Outline each blood parasite and name the species.
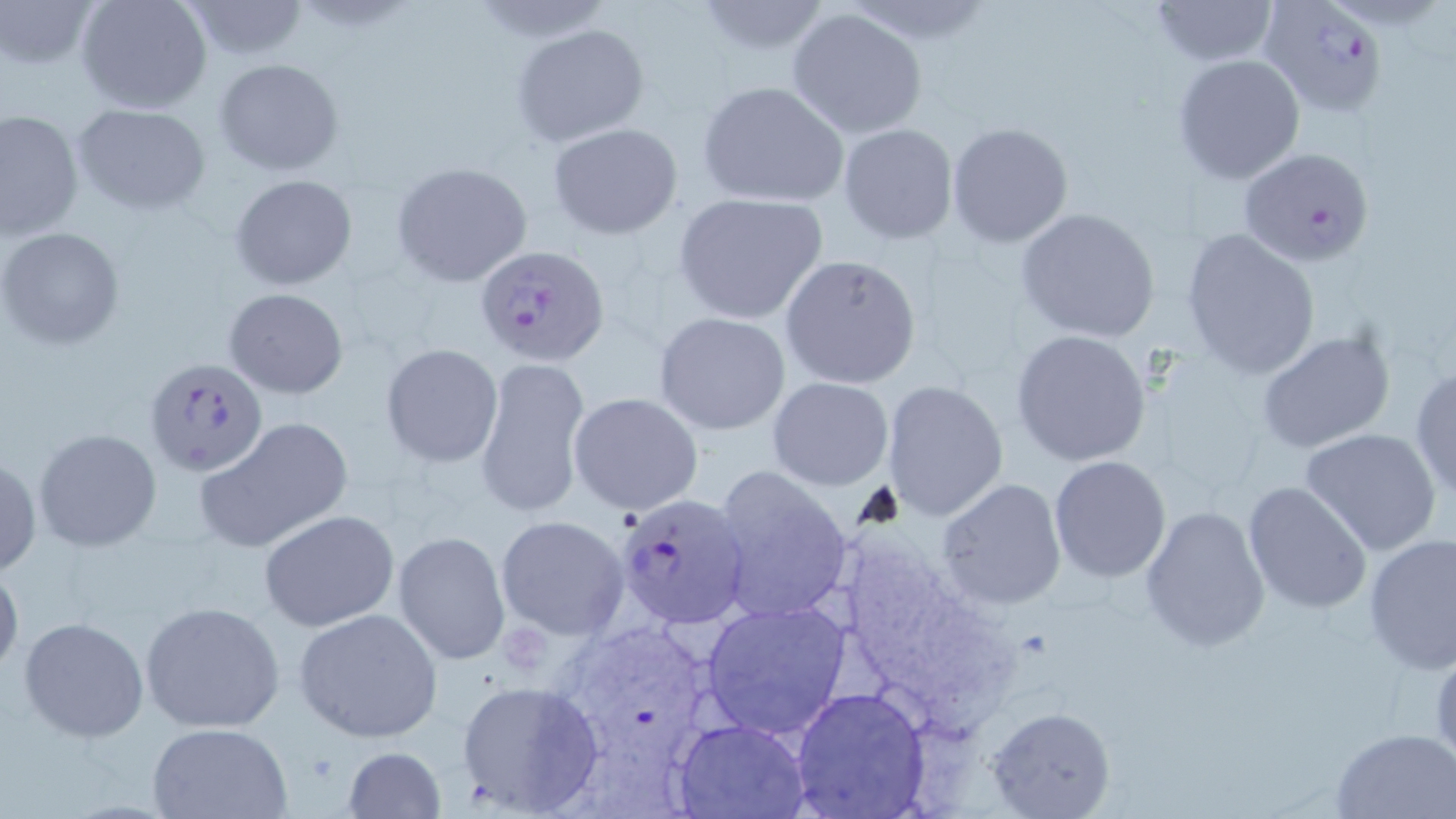

Approximate bounding boxes as (x1, y1, x2, y2) in pixels.
Plasmodium falciparum-infected red blood cells: (1260, 0, 1389, 116), (1237, 145, 1374, 265), (476, 246, 609, 366), (145, 358, 269, 476), (616, 493, 750, 629).
No Plasmodium ovale, Plasmodium malariae, Plasmodium vivax, Babesia divergens, or Trypanosoma brucei observed.

Summary:
  - Uninfected red blood cell locations: (2, 0, 103, 71), (75, 0, 213, 114), (1149, 0, 1277, 67), (179, 1, 309, 61), (690, 1, 830, 55), (788, 7, 929, 138), (513, 24, 650, 146), (1172, 53, 1305, 185), (214, 57, 344, 176), (696, 81, 849, 208), (72, 104, 210, 215), (0, 107, 84, 242), (548, 122, 684, 239), (946, 123, 1073, 248), (837, 124, 959, 244), (391, 163, 533, 287), (230, 173, 358, 290), (672, 192, 829, 325), (1014, 207, 1161, 343), (0, 226, 125, 351), (1180, 229, 1320, 379), (779, 254, 922, 389), (223, 287, 349, 400), (653, 311, 790, 435), (1257, 329, 1396, 454), (1011, 330, 1150, 466), (381, 343, 503, 467), (477, 355, 591, 522), (1409, 364, 1456, 500), (769, 377, 894, 489), (882, 381, 1009, 520), (569, 392, 704, 515), (197, 416, 354, 552), (1301, 427, 1442, 555), (33, 428, 163, 553), (1, 454, 42, 581), (1049, 457, 1170, 581), (709, 465, 852, 623), (938, 477, 1066, 610), (1242, 481, 1371, 615), (1139, 505, 1271, 654), (258, 509, 399, 632), (496, 515, 631, 640), (392, 530, 510, 667), (1363, 533, 1456, 673), (0, 560, 24, 683), (700, 599, 850, 740), (137, 600, 285, 735), (293, 608, 444, 744), (19, 616, 148, 741), (454, 679, 606, 816), (793, 688, 928, 818), (984, 705, 1115, 819), (674, 719, 809, 818), (147, 723, 293, 818), (1333, 727, 1456, 817), (340, 746, 446, 818)
  - Slide-level diagnosis: Plasmodium falciparum
  - Image size: 1456×819 pixels
  - Preparation: thin blood film
  - Modality: light microscopy
  - Magnification: 1000x
  - Field of view: single
  - Stain: May-Grünwald-Giemsa